Give the position of every leukocyte visible.
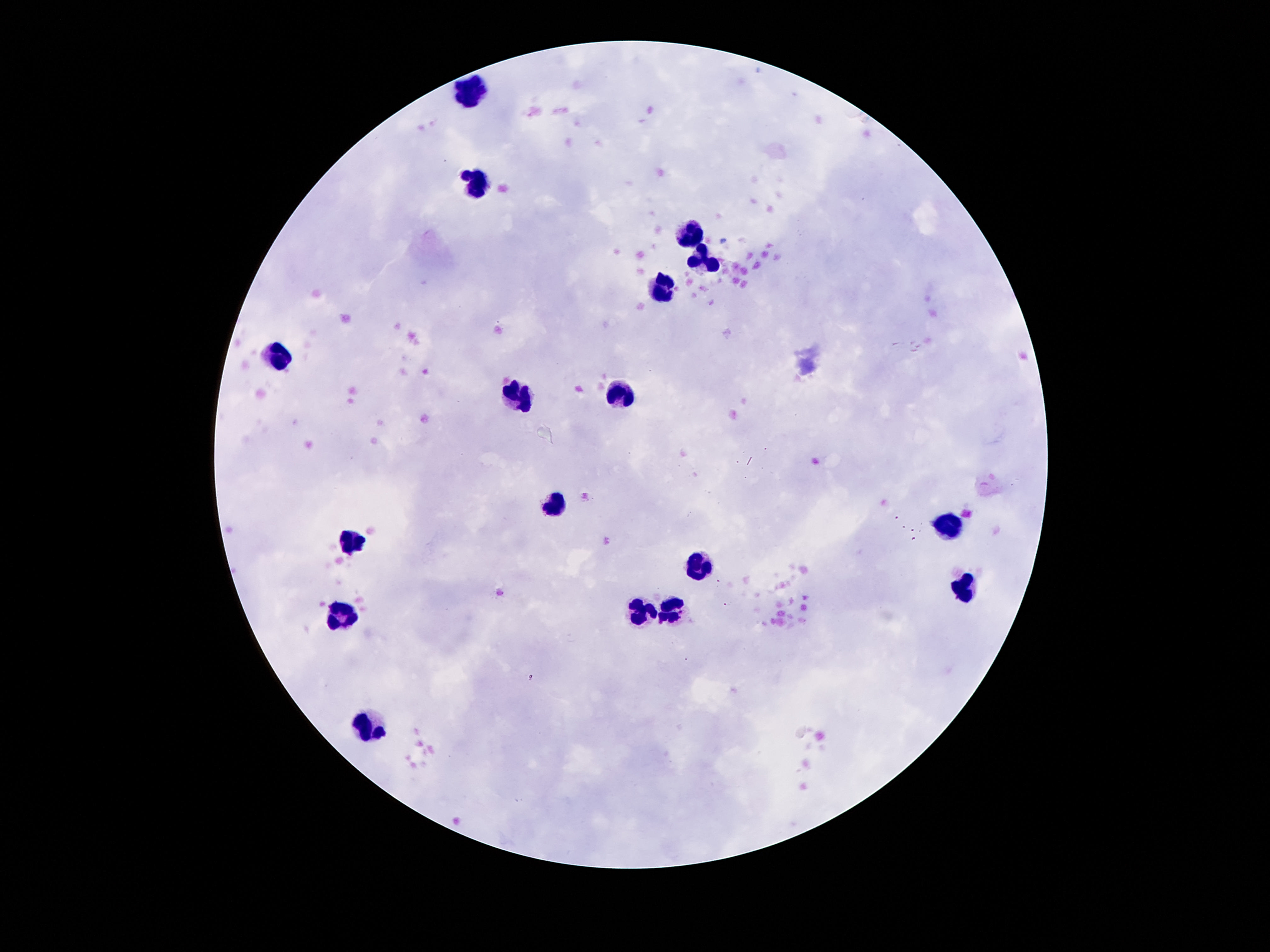
Approximate centers as (x, y) in pixels.
Leukocytes: (472, 90), (472, 187), (692, 232), (705, 258), (666, 289), (278, 355), (621, 395), (519, 398), (554, 501), (946, 527), (353, 540), (700, 567), (966, 589), (640, 612), (343, 615), (672, 617), (371, 727).

Summary:
  - Field of view: one from this slide
  - Patient malaria status: negative
  - Image size: 1270×952 pixels
  - Capture: smartphone camera through the microscope eyepiece
  - Magnification: 100x
  - Stain: Giemsa
  - Preparation: thick blood smear